Assess the morphology of the erythrocytes.
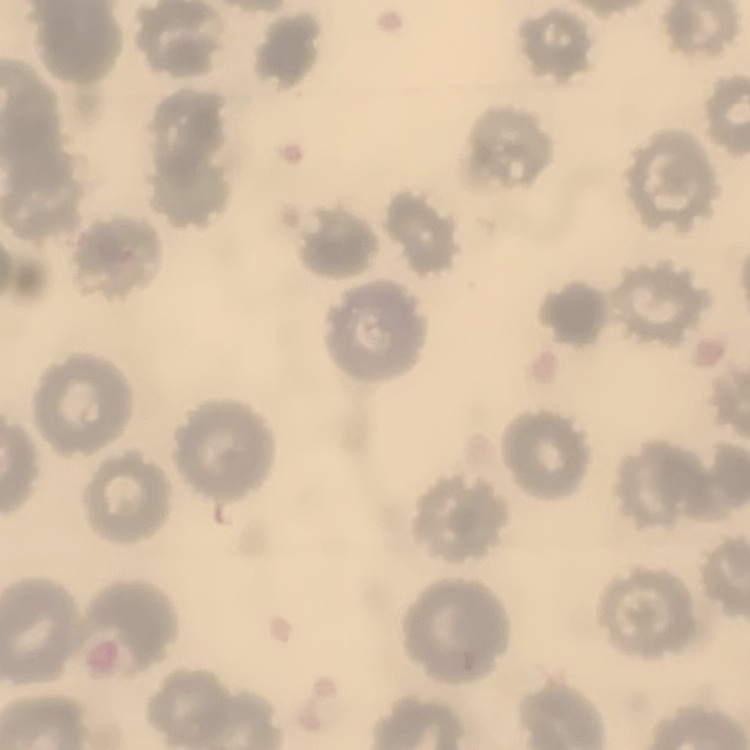

No rouleaux formation.

image_type: square crop of a larger photomicrograph
preparation: thin blood film
stain: Field's or Giemsa